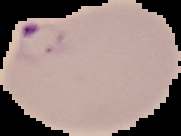 Image is 181×136 pixels. Segmented cell region on a black background. Result: malaria parasites detected. From a thin blood smear.